Assess this cell for malaria.
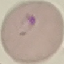

It is parasitized.

Giemsa-stained preparation. Thin blood film. Acquired by smartphone through the microscope eyepiece. Cell patch, automatically extracted from a larger field of view and resized to 64 × 64 pixels.